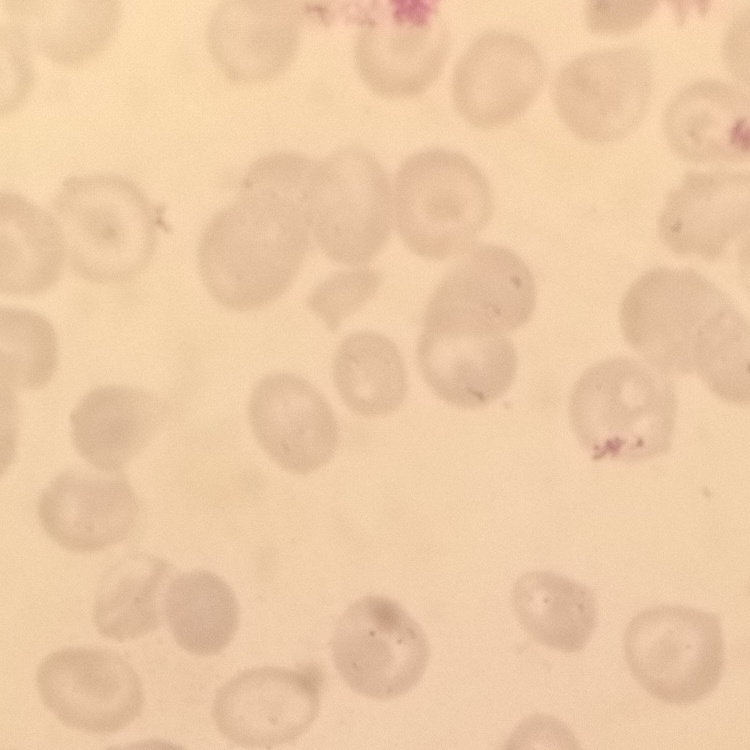
Summary:
  - Erythrocyte morphology: no rouleaux formation
  - Preparation: thin blood film
  - Image type: one tile cut from a larger photomicrograph
  - Stain: Field's or Giemsa